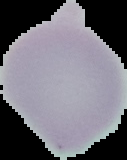
Summary:
  - Image size: 127×160 pixels
  - Malaria status: uninfected
  - Preparation: thin blood film
  - Image type: cell region segmented out of the field of view; surrounding area masked to black